Assess this cell for malaria.
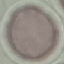

Uninfected.

image type = automatically extracted cell patch, resized to 64 × 64 pixels
stain = Giemsa
preparation = thin smear
capture = smartphone through the microscope eyepiece